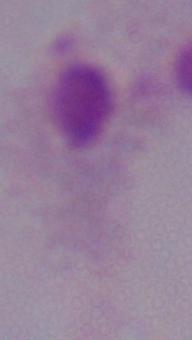

magnification = 1000x
identification = trichomonad
modality = micrograph